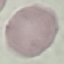

Result: no malaria parasites detected. Photographed with a smartphone camera at the microscope eyepiece. Thin blood film. Cell patch, automatically extracted from a larger field of view and resized to 64 × 64 pixels. Giemsa-stained preparation.